Locate every Plasmodium parasite.
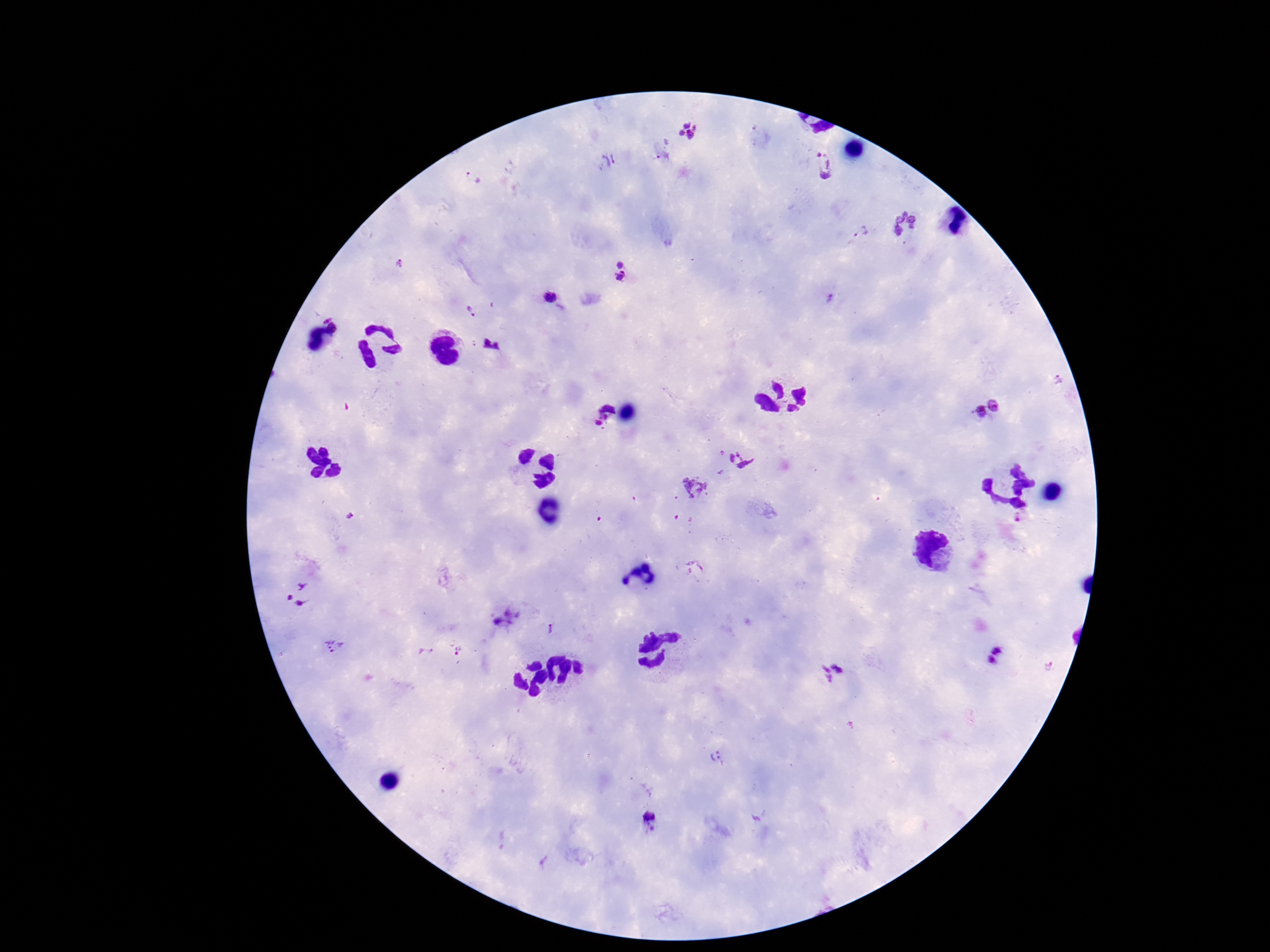
Approximate object centers, in pixels from the top-left corner.
Plasmodium parasites: (x=688, y=130), (x=662, y=157), (x=607, y=160), (x=823, y=163), (x=474, y=178), (x=903, y=224), (x=861, y=232), (x=398, y=264), (x=622, y=272), (x=550, y=298), (x=830, y=298), (x=468, y=309), (x=1058, y=379), (x=985, y=408), (x=600, y=420), (x=721, y=453), (x=740, y=458), (x=720, y=472), (x=694, y=487), (x=298, y=594), (x=508, y=617), (x=551, y=629), (x=334, y=647), (x=458, y=650), (x=424, y=652), (x=996, y=657), (x=832, y=673), (x=718, y=757), (x=651, y=821).

Summary:
  - Magnification: 100x
  - Patient malaria status: positive
  - Field of view: single
  - Image size: 1270×952 pixels
  - Stain: Giemsa
  - Preparation: thick blood smear
  - Capture: smartphone camera through the microscope eyepiece